Identify the parasite.
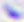

Toxoplasma gondii.

modality = micrograph
magnification = 400x